Report the malaria status of this cell.
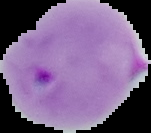
It is parasitized.

From a thin blood smear. Cell region segmented out of the field of view; the surrounding area is masked to black. Image is 151×133 pixels.